State which parasite is depicted.
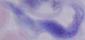

A trypanosome.

Micrograph. 1000x magnification.